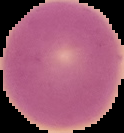 Image is 124×133 pixels. From a thin blood film. Result: negative for malaria parasites. Cell region segmented out of the field of view; the surrounding area is masked to black.